Assess this cell for malaria.
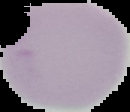
It is uninfected.

The area outside the segmented cell region is set to black. From a thin blood smear. Image is 130×112 pixels.